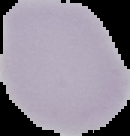
Image is 130×136 pixels. From a thin blood film. Segmented cell region on a black background. Malaria status: uninfected.